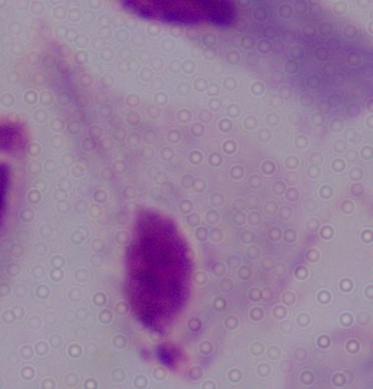

A trichomonad is seen. Captured at 1000x magnification. Micrograph.